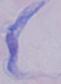
magnification = 1000x
identification = trypanosome
modality = micrograph